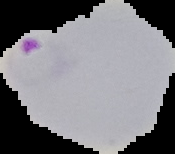

Summary:
  - Image size: 175×154 pixels
  - Image type: segmented cell region with the area outside set to black
  - Result: malaria parasites identified
  - Preparation: thin blood smear